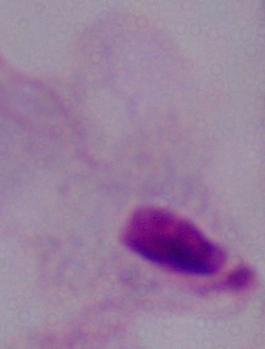
A trichomonad is shown. Micrograph. 1000x magnification.